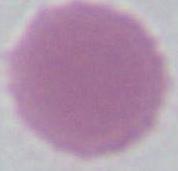

identification = erythrocyte
magnification = 1000x
modality = micrograph